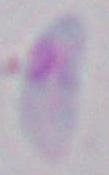
modality = micrograph
identification = Toxoplasma gondii
magnification = 1000x